Report the malaria status of this cell.
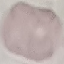
It is uninfected.

Summary:
  - Capture: smartphone camera at the microscope eyepiece
  - Stain: Giemsa
  - Image type: automatically extracted cell patch, resized to 64 × 64 pixels
  - Preparation: thin blood smear